Locate and identify every blood parasite.
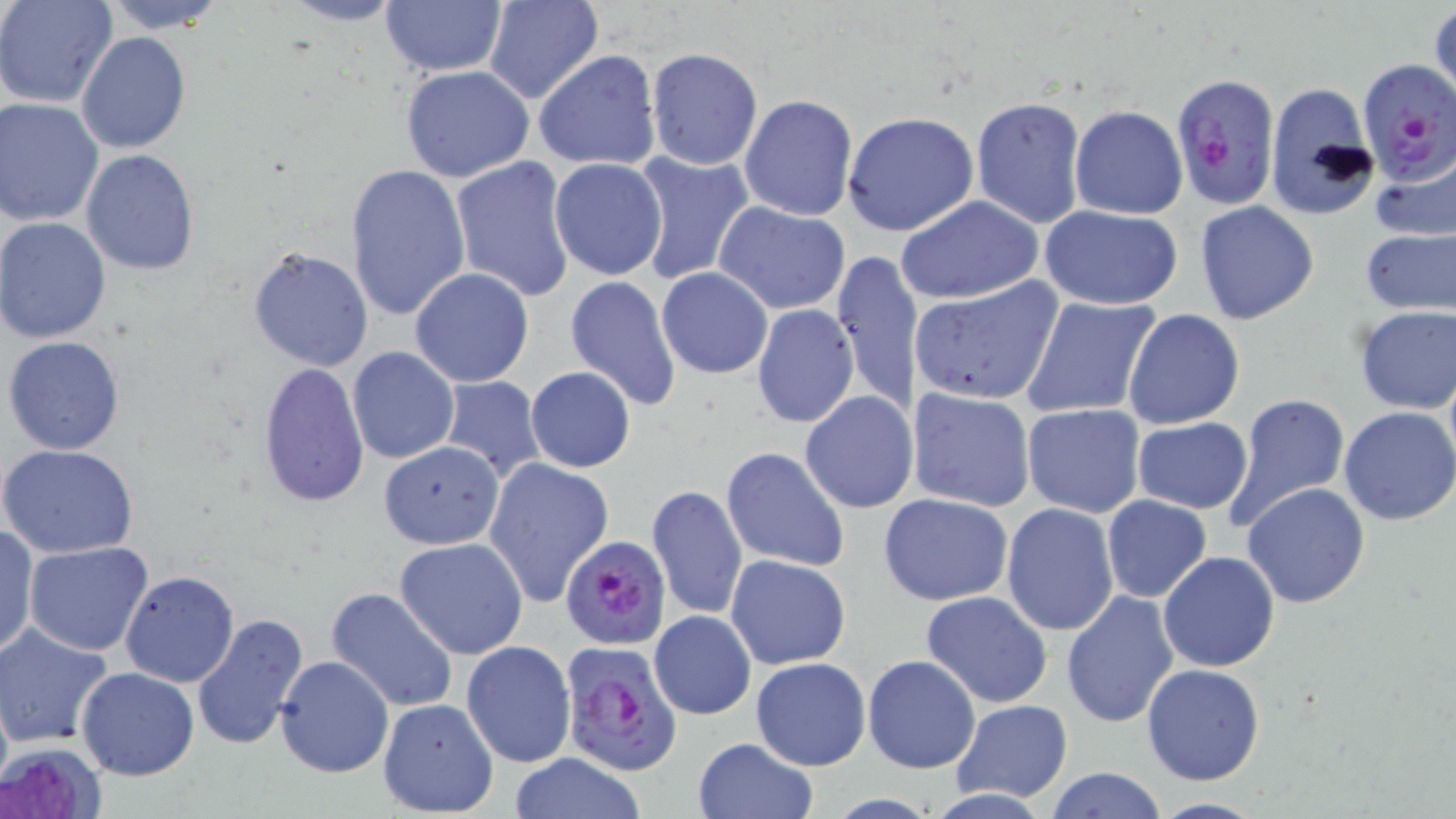
Approximate bounding boxes as [x1, y1, x2, y2] in pixels.
Plasmodium falciparum-infected red blood cells: [1357, 60, 1456, 184], [1172, 73, 1281, 214], [558, 534, 673, 650], [559, 641, 683, 774].
No Plasmodium ovale, Plasmodium malariae, Plasmodium vivax, Babesia divergens, or Trypanosoma brucei observed.

Uninfected red blood cell locations: [0, 0, 119, 108], [99, 0, 232, 35], [481, 0, 602, 105], [279, 1, 408, 27], [379, 1, 506, 77], [1428, 4, 1456, 107], [77, 33, 190, 154], [645, 48, 763, 172], [533, 51, 662, 171], [400, 64, 536, 183], [1262, 82, 1379, 221], [738, 94, 858, 220], [970, 95, 1087, 229], [0, 97, 104, 227], [1070, 105, 1188, 219], [842, 111, 979, 236], [79, 149, 200, 275], [628, 150, 755, 287], [1370, 151, 1456, 242], [449, 155, 575, 303], [548, 158, 667, 281], [345, 162, 470, 321], [896, 196, 1044, 304], [714, 200, 852, 315], [1194, 201, 1320, 324], [1040, 206, 1184, 310], [0, 217, 112, 344], [1358, 225, 1455, 319], [248, 245, 376, 372], [832, 249, 925, 418], [408, 267, 535, 388], [657, 267, 773, 379], [564, 275, 682, 413], [909, 276, 1066, 408], [1021, 295, 1162, 421], [1352, 303, 1456, 414], [752, 304, 860, 427], [1122, 310, 1245, 430], [3, 336, 127, 456], [346, 345, 460, 465], [255, 362, 371, 512], [525, 367, 636, 473], [436, 375, 545, 485], [906, 387, 1037, 511], [800, 390, 918, 512], [1224, 393, 1351, 531], [1023, 404, 1145, 517], [1337, 407, 1456, 526], [1132, 418, 1253, 514], [378, 440, 505, 550], [0, 444, 140, 559], [721, 446, 851, 572], [483, 456, 615, 608], [1241, 483, 1370, 608], [647, 484, 748, 622], [878, 492, 1015, 606], [1102, 495, 1211, 602], [1001, 503, 1119, 636], [0, 524, 38, 661], [1012, 537, 1139, 694], [395, 538, 528, 659], [24, 541, 155, 656], [1158, 551, 1281, 673], [724, 553, 851, 671], [120, 571, 240, 686], [324, 586, 459, 714], [920, 590, 1054, 708], [1061, 591, 1178, 728], [651, 610, 755, 718], [190, 613, 309, 751], [0, 623, 113, 747], [462, 640, 576, 767], [274, 655, 394, 776], [750, 656, 871, 771], [862, 656, 981, 772], [1141, 663, 1267, 786], [77, 667, 200, 780], [378, 698, 499, 817], [952, 700, 1072, 802], [692, 736, 817, 819], [1, 740, 109, 819], [504, 754, 651, 818], [1045, 765, 1168, 819], [1144, 797, 1272, 819]. Slide-level diagnosis: Plasmodium falciparum. Image is 1456×819 pixels. 1000x magnification. Thin blood film. Single field of view. May-Grünwald-Giemsa-stained preparation. Optical microscopy.